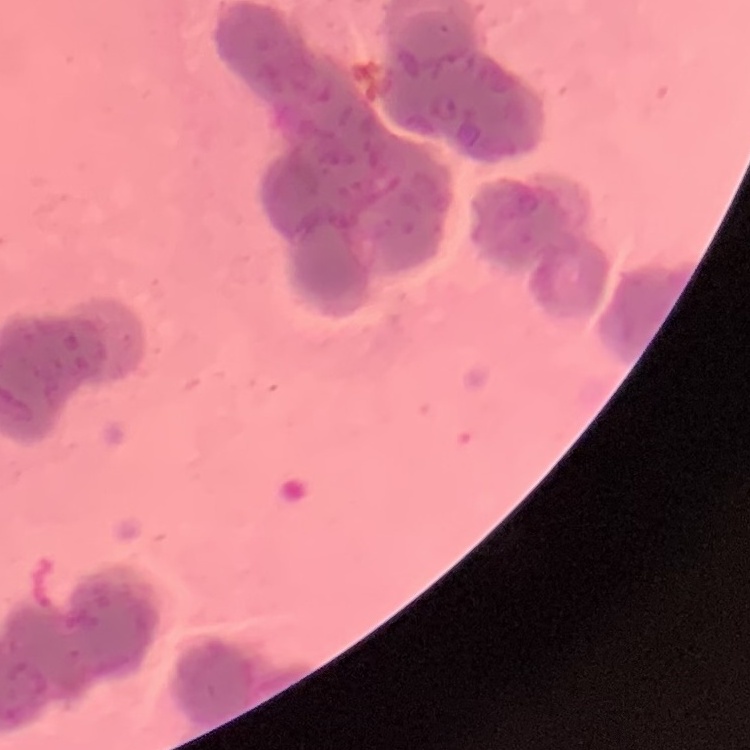 The red blood cells exhibit rouleaux formation. One tile cut from a larger photomicrograph. Thin peripheral smear. Field's or Giemsa stain.